Assess this cell for malaria.
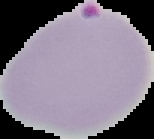

Parasitized.

Summary:
  - Image size: 154×139 pixels
  - Preparation: thin blood smear
  - Image type: segmented cell region on a black background